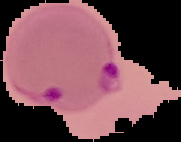
image type = segmented cell region with the area outside set to black
malaria status = parasitized
image size = 181×142 pixels
preparation = thin blood smear